State the preparation type.
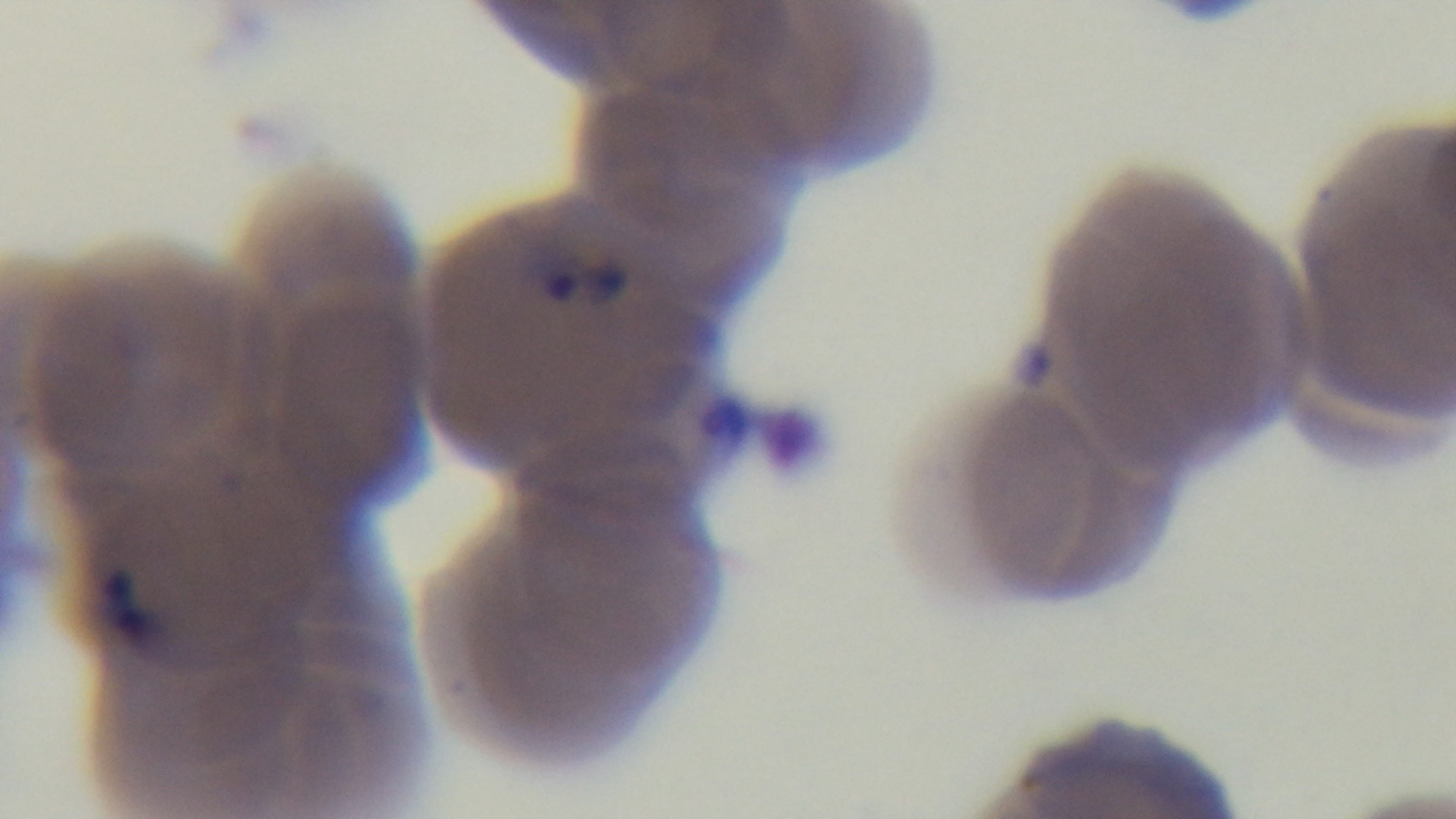

It is a thin blood film.

modality = light microscopy
field of view = one from the slide
stain = Giemsa
objective = 100x oil immersion
malaria status = infected
capture = mounted 4K digital camera